State which parasite is depicted.
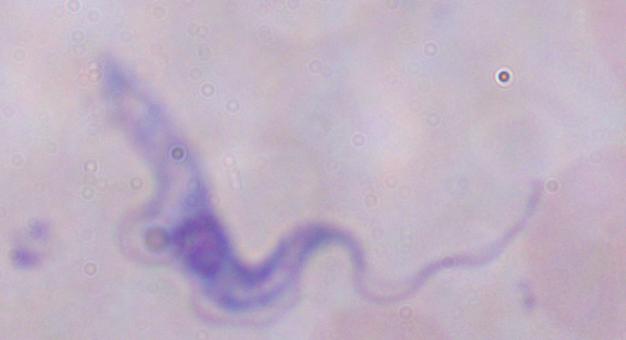
This is a trypanosome.

Photomicrograph. Captured at 1000x magnification.